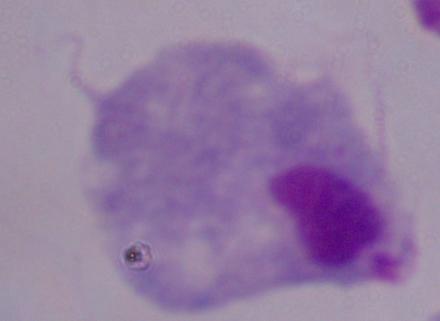
magnification = 1000x
identification = trichomonad
modality = photomicrograph